Identify the preparation type.
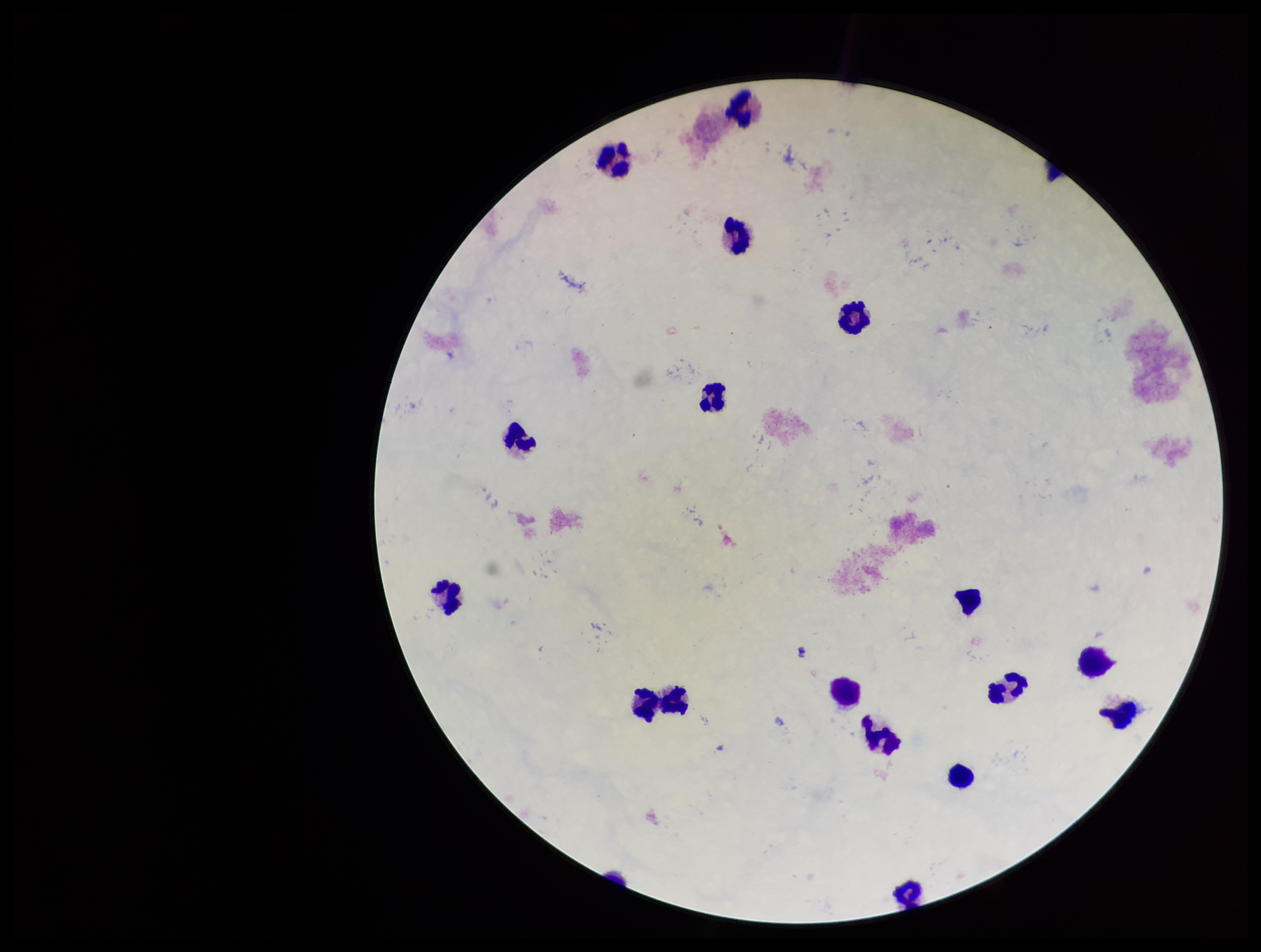
A thick smear.

Leukocyte count: 16. Plasmodium parasites: none seen. Photographed through the microscope eyepiece with a smartphone camera. Stained with Giemsa. Parasite count: 0. Image is 1261×952 pixels. Single field of view. Patient malaria status: negative.